Assess for Plasmodium parasites.
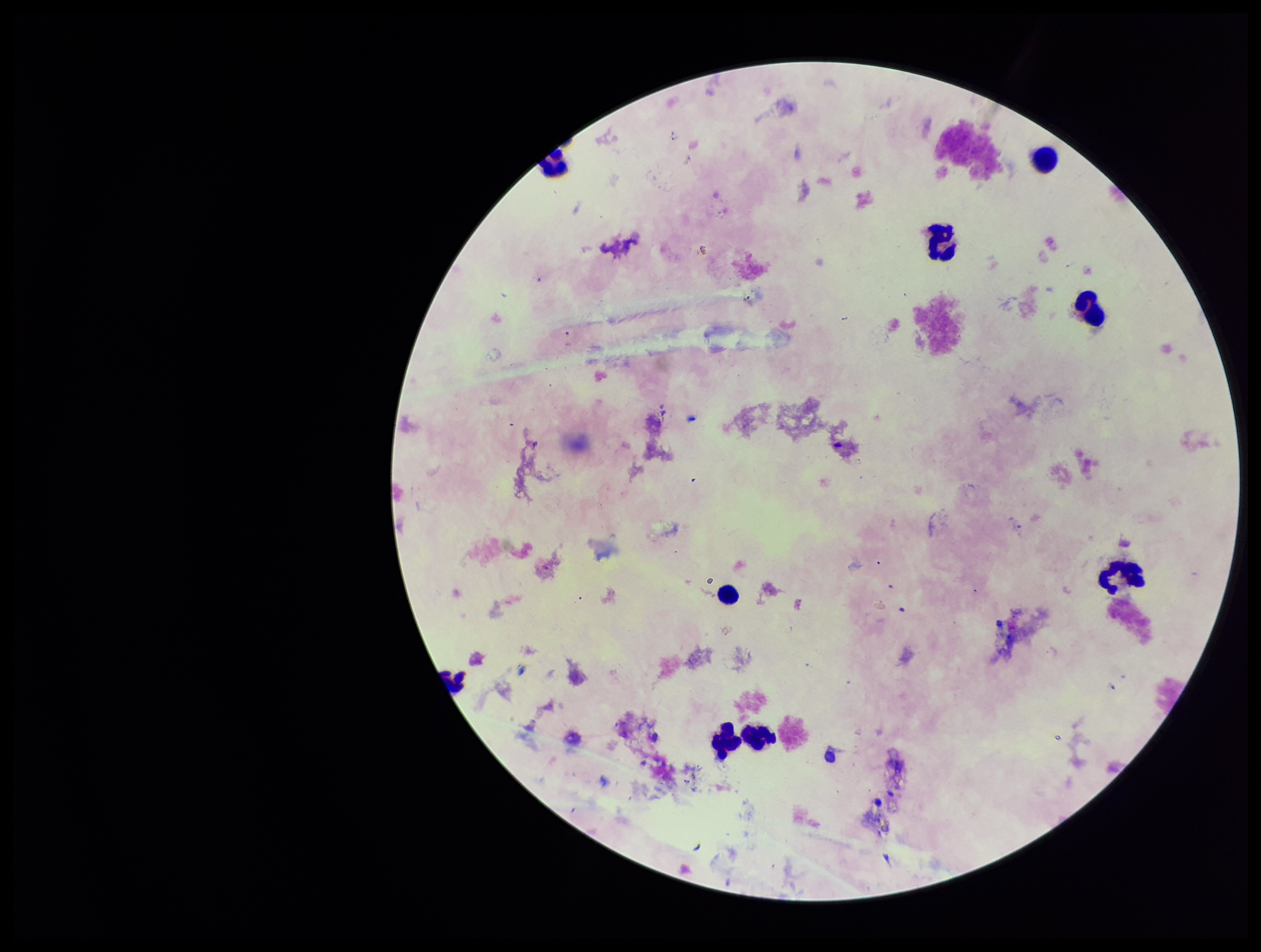

None seen.

Preparation: thick blood smear. Leukocyte count: 9. Photographed through the microscope eyepiece with a smartphone camera. Parasite count: 0. Image is 1261×952 pixels. Stained with Giemsa. Patient malaria status: negative. Single field of view.